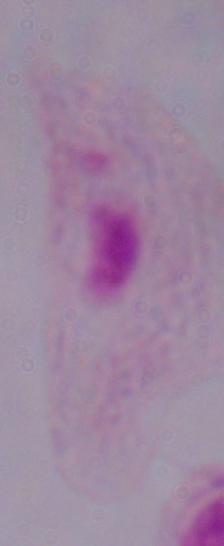
Summary:
  - Identification: trichomonad
  - Magnification: 1000x
  - Modality: photomicrograph